Identify the blood parasite species.
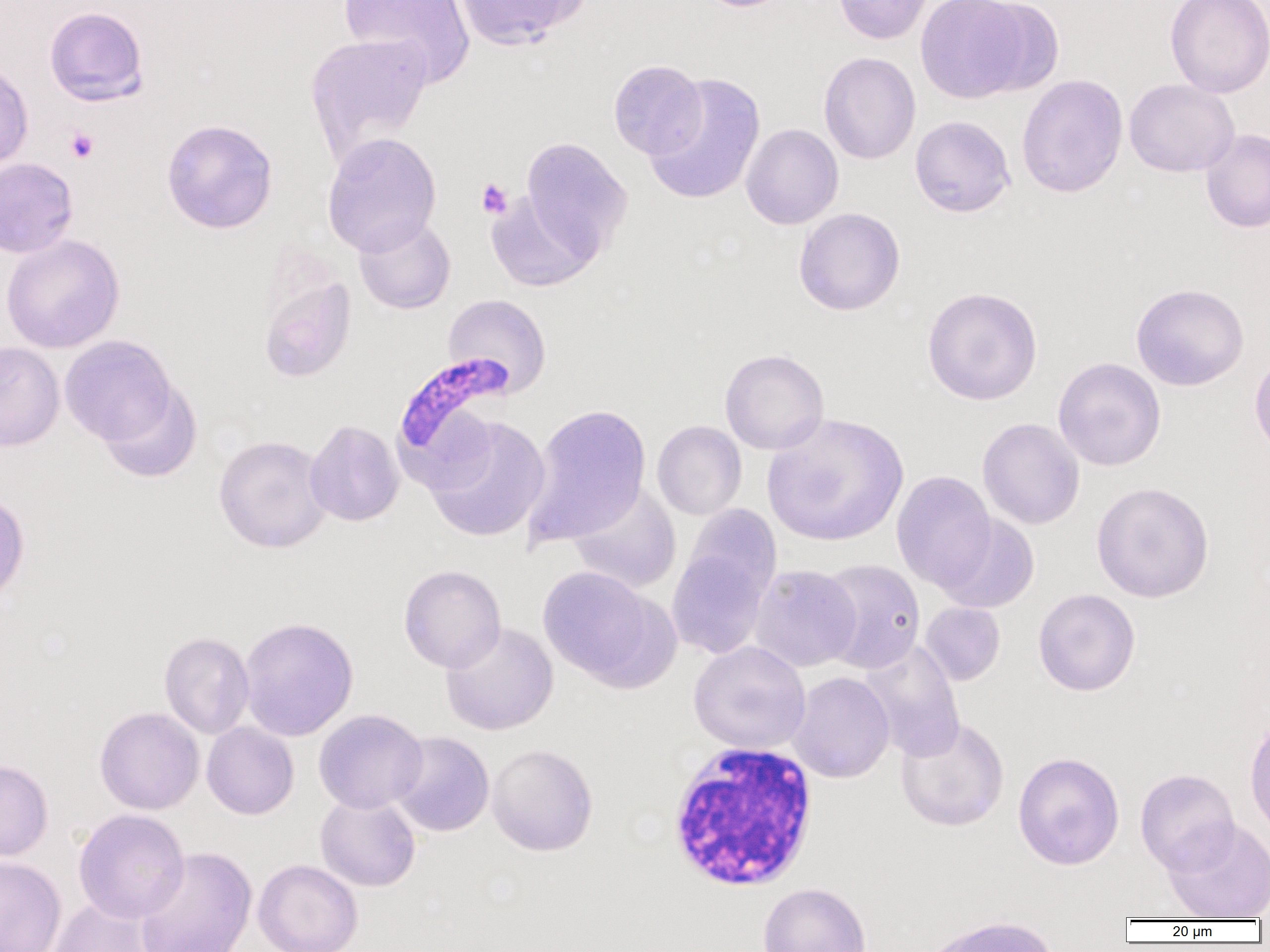
Plasmodium falciparum.

{
  "white_blood_cell_locations": "approximate bounding boxes as [x1, y1, x2, y2] in pixels: [665, 742, 819, 892]",
  "image_size": "1270×952 pixels",
  "preparation": "thin blood film",
  "platelet_locations": "approximate bounding boxes as [x1, y1, x2, y2] in pixels: [65, 127, 98, 163], [476, 177, 514, 220]",
  "plasmodium_falciparum_infected_red_blood_cell_locations": "approximate bounding boxes as [x1, y1, x2, y2] in pixels: [393, 352, 515, 474]",
  "modality": "optical microscopy",
  "uninfected_red_blood_cell_locations": "approximate bounding boxes as [x1, y1, x2, y2] in pixels: [339, 0, 475, 88], [453, 0, 588, 49], [693, 0, 797, 12], [833, 0, 933, 44], [915, 0, 1030, 103], [971, 0, 1065, 96], [1164, 0, 1270, 98], [44, 6, 149, 106], [305, 32, 432, 166], [819, 52, 921, 165], [608, 59, 707, 159], [0, 60, 33, 171], [644, 72, 766, 206], [1016, 74, 1129, 199], [1124, 78, 1239, 178], [909, 115, 1016, 218], [161, 119, 278, 234], [740, 123, 844, 229], [1200, 128, 1270, 234], [321, 132, 442, 257], [519, 137, 633, 257], [0, 157, 78, 258], [486, 192, 600, 292], [793, 208, 906, 316], [354, 215, 455, 314], [1, 234, 125, 353], [257, 266, 357, 385], [1130, 283, 1249, 391], [922, 285, 1043, 406], [443, 294, 552, 397], [59, 335, 177, 447], [0, 341, 65, 451], [719, 348, 829, 455], [1249, 351, 1270, 461], [1053, 357, 1166, 471], [97, 377, 202, 483], [522, 403, 651, 547], [762, 412, 909, 548], [424, 415, 550, 543], [977, 418, 1085, 530], [305, 419, 405, 527], [652, 420, 747, 521], [213, 434, 333, 553], [892, 470, 996, 591], [1091, 481, 1215, 603], [566, 483, 682, 593], [0, 491, 30, 607], [682, 505, 782, 606], [934, 513, 1040, 614], [666, 545, 772, 659], [817, 559, 925, 674], [749, 564, 862, 672], [398, 565, 506, 673], [537, 565, 663, 686], [1033, 589, 1140, 696], [919, 602, 1005, 686], [238, 616, 359, 742], [440, 621, 558, 736], [159, 631, 255, 739], [857, 640, 966, 760], [688, 641, 811, 755], [788, 671, 895, 783], [94, 707, 204, 815], [313, 709, 428, 814], [1244, 715, 1270, 841], [895, 716, 1009, 832], [202, 722, 299, 819], [390, 731, 495, 837], [487, 743, 598, 856], [1013, 751, 1125, 870], [0, 759, 53, 862], [1135, 768, 1240, 876], [315, 793, 421, 892], [72, 808, 190, 924], [1163, 818, 1270, 920], [134, 846, 256, 952], [0, 855, 67, 952], [253, 859, 363, 952], [758, 882, 871, 952], [46, 898, 158, 952], [923, 915, 1059, 952]",
  "field_of_view": "single",
  "magnification": "1000x"
}